Find the red blood cells and label each as P. falciparum-infected, uninfected, or of indeterminate infection status.
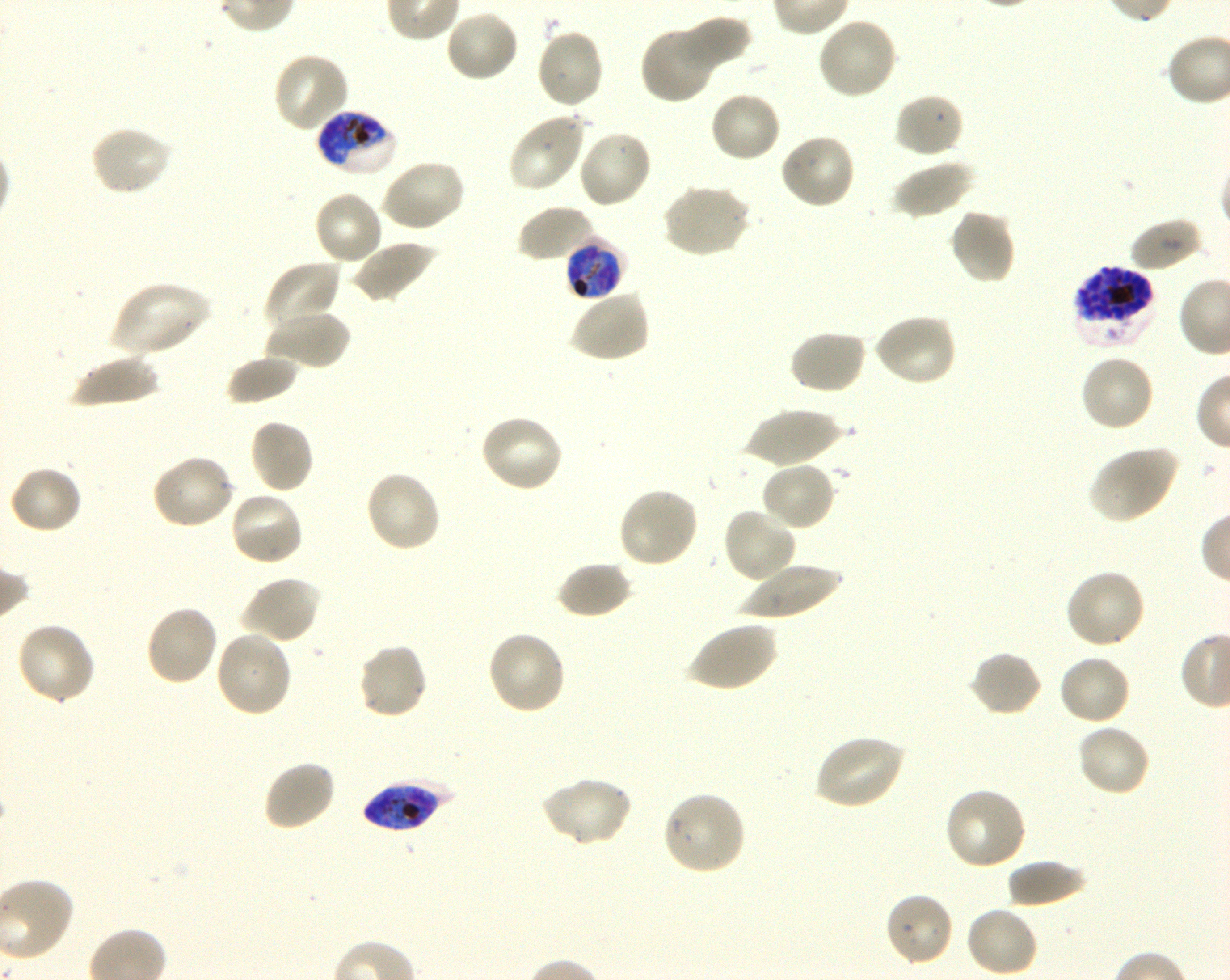

Approximate bounding boxes as {x1, y1, x2, y2} in pixels. Not every red blood cell is marked. A life-cycle stage — or a range of stages, where the recorded stages span more than one — follows each staged infected red blood cell.
Infected red blood cells: {314, 109, 397, 177} late trophozoite to late schizont; {564, 238, 627, 301} late trophozoite to early schizont; {1072, 265, 1157, 348} schizont; {361, 779, 454, 832}.
Uninfected red blood cells: {445, 9, 520, 83}, {676, 16, 751, 74}, {816, 16, 898, 101}, {639, 23, 718, 104}, {535, 26, 606, 109}, {272, 51, 350, 134}, {708, 91, 783, 163}, {893, 92, 965, 158}, {508, 110, 587, 193}, {89, 124, 173, 198}, {577, 129, 653, 209}, {779, 132, 857, 211}, {380, 159, 466, 233}, {891, 159, 974, 220}, {661, 183, 750, 258}, {312, 191, 385, 267}, {518, 204, 596, 263}, {949, 209, 1016, 285}, {1128, 217, 1204, 273}, {349, 240, 438, 304}, {264, 260, 344, 334}, {110, 280, 211, 358}, {570, 287, 650, 363}, {264, 309, 350, 371}, {873, 312, 958, 387}, {788, 329, 867, 395}, {225, 353, 299, 405}, {67, 354, 161, 407}, {1078, 354, 1156, 433}, {743, 409, 843, 467}, {479, 414, 565, 494}, {249, 418, 315, 494}, {1088, 445, 1179, 524}, {150, 453, 236, 531}, {760, 460, 837, 532}, {8, 465, 83, 535}, {364, 470, 442, 553}, {617, 486, 700, 570}, {229, 490, 305, 567}, {722, 506, 798, 584}, {556, 560, 632, 619}, {738, 562, 844, 619}, {1064, 569, 1146, 650}, {240, 575, 321, 645}, {144, 604, 219, 687}, {686, 620, 777, 693}, {15, 621, 96, 705}, {214, 629, 293, 718}, {486, 629, 567, 715}, {356, 642, 429, 720}, {969, 650, 1043, 717}, {1057, 654, 1131, 727}, {1076, 722, 1151, 798}, {813, 734, 906, 810}, {262, 759, 337, 832}, {539, 776, 633, 847}, {944, 786, 1027, 870}, {661, 790, 747, 876}, {1005, 859, 1088, 908}, {883, 891, 954, 967}, {964, 905, 1040, 978}.
No red blood cells of indeterminate infection status observed.

field of view = single
image size = 1230×980 pixels
donor blood group = O+
culture = shaking in-vitro P. falciparum strain 3D7
stain = Giemsa
preparation = thin blood film
objective = 100x, oil immersion, numerical aperture 1.30